Assess this cell for malaria.
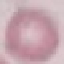

Uninfected.

Summary:
  - Capture: smartphone through the microscope eyepiece
  - Stain: Giemsa
  - Preparation: thin blood smear
  - Image type: automatically extracted cell patch, resized to 64 × 64 pixels